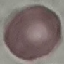

malaria status = uninfected
image type = cell patch, automatically extracted from a larger field of view and resized to 64 × 64 pixels
capture = smartphone through the microscope eyepiece
stain = Giemsa
preparation = thin blood smear